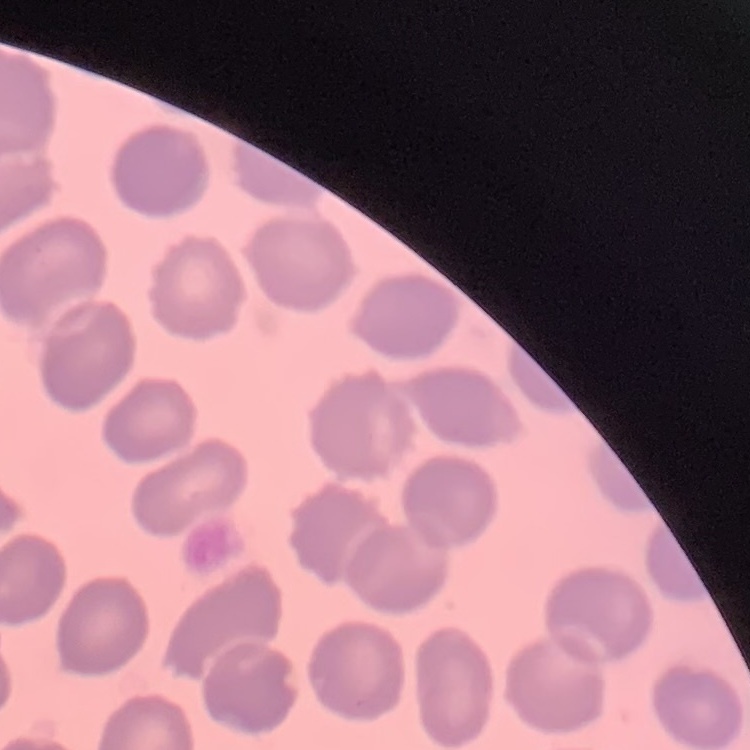 The erythrocytes exhibit no rouleaux formation. Stained with either Field's or Giemsa. Square crop of a larger photomicrograph. Thin blood film.